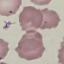

Result: no malaria parasites detected. Photographed with a smartphone camera at the microscope eyepiece. Cell patch, automatically extracted from a larger field of view and resized to 64 × 64 pixels. Giemsa-stained preparation. Thin blood film.